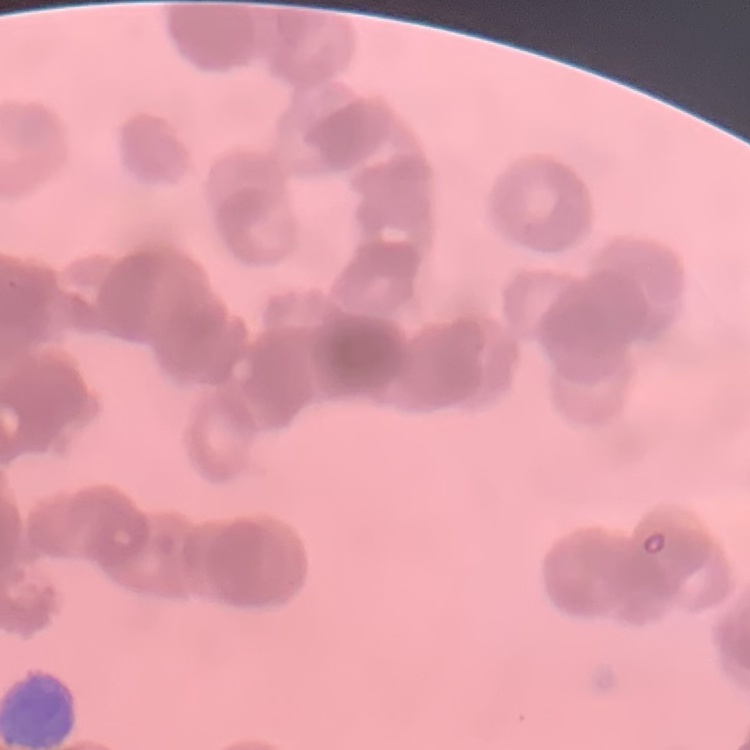

erythrocyte_morphology: rouleaux formation
preparation: thin blood smear
image_type: one tile cut from a larger photomicrograph
stain: Field's or Giemsa